State which parasite is depicted.
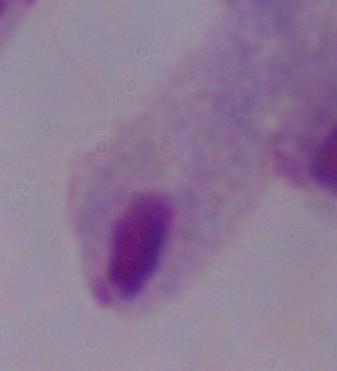
A trichomonad.

{
  "modality": "micrograph",
  "magnification": "1000x"
}